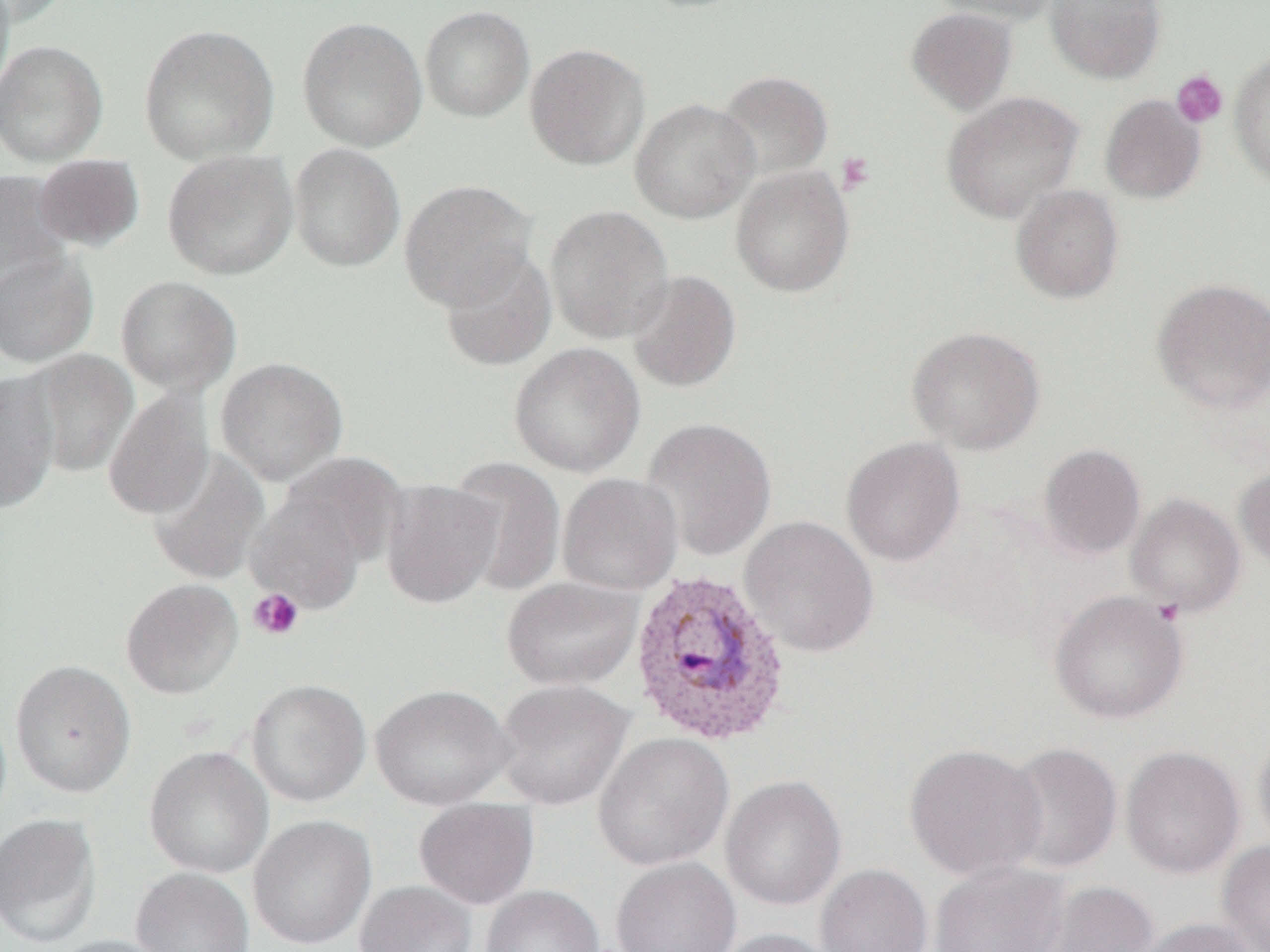

Approximate bounding boxes as (x1, y1, x2, y2) in pixels. Plasmodium vivax-infected red blood cell locations: (628, 566, 792, 746). Uninfected red blood cell locations: (0, 0, 15, 103), (1, 0, 67, 28), (926, 0, 1063, 25), (1045, 0, 1167, 84), (420, 5, 534, 122), (906, 7, 1017, 114), (297, 16, 428, 152), (138, 23, 280, 164), (0, 40, 108, 166), (524, 43, 650, 170), (1228, 51, 1270, 186), (715, 70, 833, 182), (940, 91, 1083, 222), (1100, 94, 1205, 203), (630, 98, 760, 224), (288, 142, 405, 272), (162, 150, 298, 280), (33, 153, 145, 252), (730, 166, 854, 297), (0, 169, 73, 291), (399, 178, 538, 310), (1011, 185, 1124, 303), (544, 204, 674, 343), (438, 248, 557, 372), (0, 251, 98, 367), (626, 270, 742, 393), (116, 275, 241, 396), (1151, 278, 1270, 413), (906, 326, 1046, 454), (508, 342, 645, 477), (25, 349, 138, 477), (215, 356, 348, 484), (0, 371, 60, 515), (102, 387, 214, 521), (640, 417, 777, 562), (841, 437, 965, 566), (1038, 443, 1146, 560), (147, 448, 270, 586), (278, 453, 406, 569), (447, 457, 567, 596), (1235, 465, 1270, 572), (557, 473, 683, 596), (379, 479, 503, 610), (246, 489, 369, 613), (1124, 493, 1246, 617), (739, 515, 879, 657), (501, 575, 644, 691), (120, 578, 244, 699), (1049, 590, 1188, 724), (11, 660, 136, 798), (246, 678, 371, 807), (492, 678, 634, 811), (370, 684, 514, 810), (1253, 727, 1270, 858), (592, 732, 734, 870), (904, 742, 1047, 881), (1002, 742, 1123, 875), (144, 745, 274, 878), (1121, 745, 1245, 879), (721, 774, 846, 911), (414, 798, 540, 909), (0, 812, 102, 948), (248, 814, 376, 949), (1217, 840, 1270, 952), (611, 857, 741, 951), (930, 862, 1068, 952), (815, 863, 932, 952), (131, 867, 255, 952), (354, 880, 477, 952), (1035, 881, 1158, 951), (480, 885, 604, 952), (1137, 917, 1264, 952), (715, 927, 839, 952), (48, 935, 173, 952). Platelet locations: (1171, 69, 1229, 128), (835, 152, 875, 194), (248, 588, 305, 640). Slide-level diagnosis: Plasmodium vivax. 1000x magnification. Light microscopy. One field of a larger specimen. Thin blood film. Image is 1270×952 pixels.